Give the preparation type.
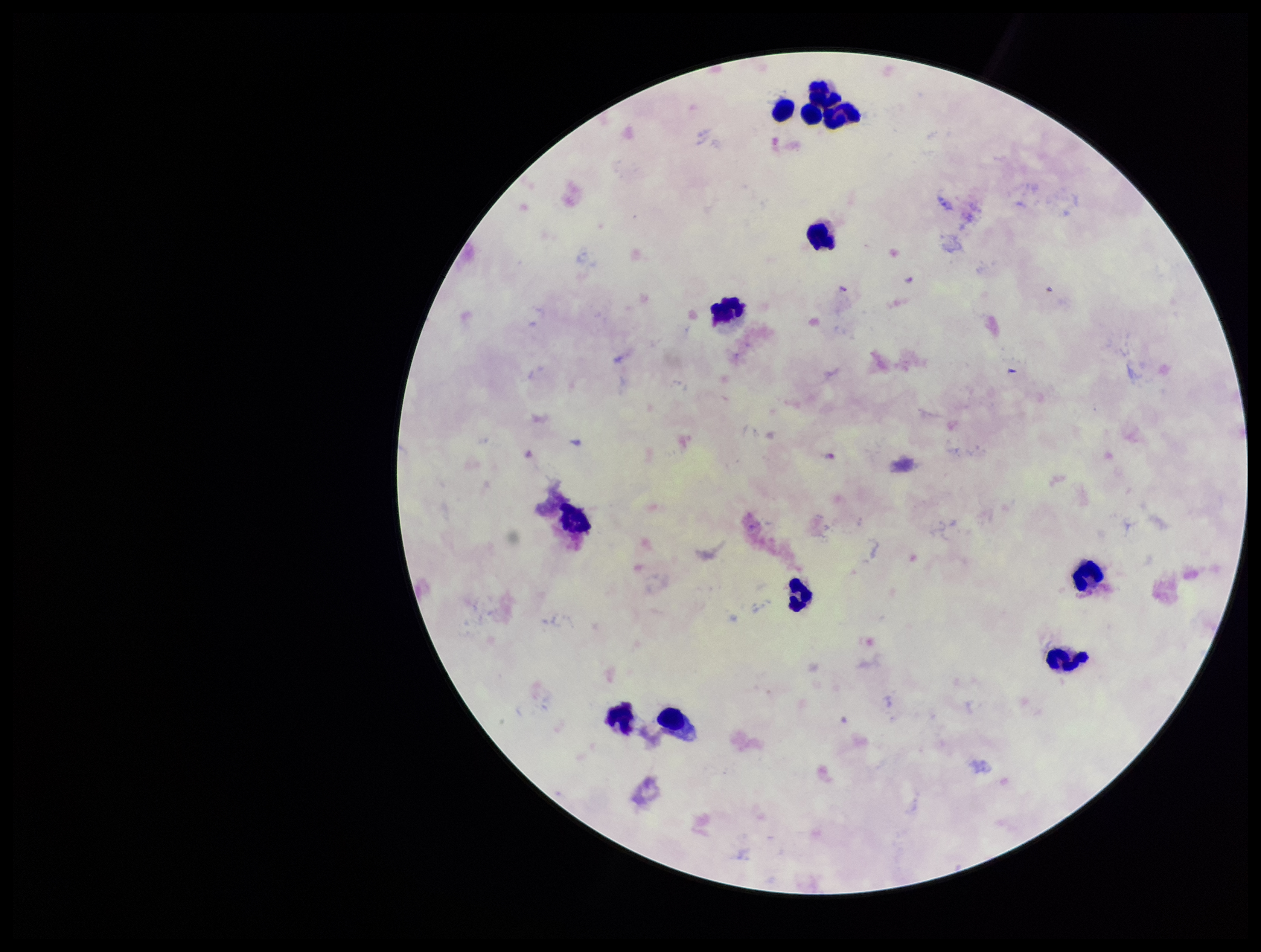
It is a thick blood smear.

Species reported for this patient: Plasmodium falciparum. Leukocyte count: 12. Patient malaria status: positive. One field from this slide. Giemsa stain. Parasite count: 3. Image is 1261×952 pixels. Plasmodium parasites: identified. Photographed through the microscope eyepiece with a smartphone camera.